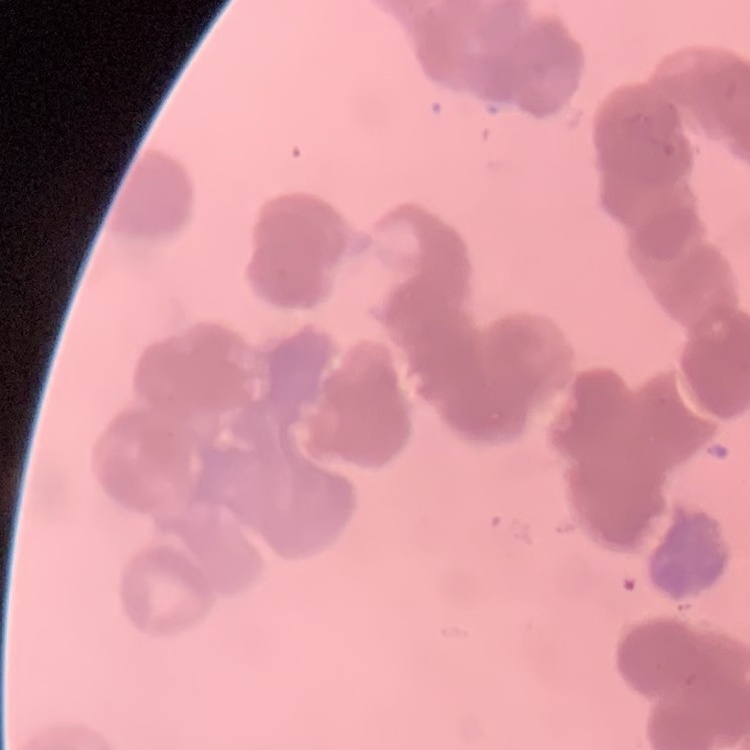 The erythrocytes exhibit rouleaux formation. Thin peripheral smear. Square crop of a larger photomicrograph. Field's or Giemsa stain.